Assess the morphology of the erythrocytes.
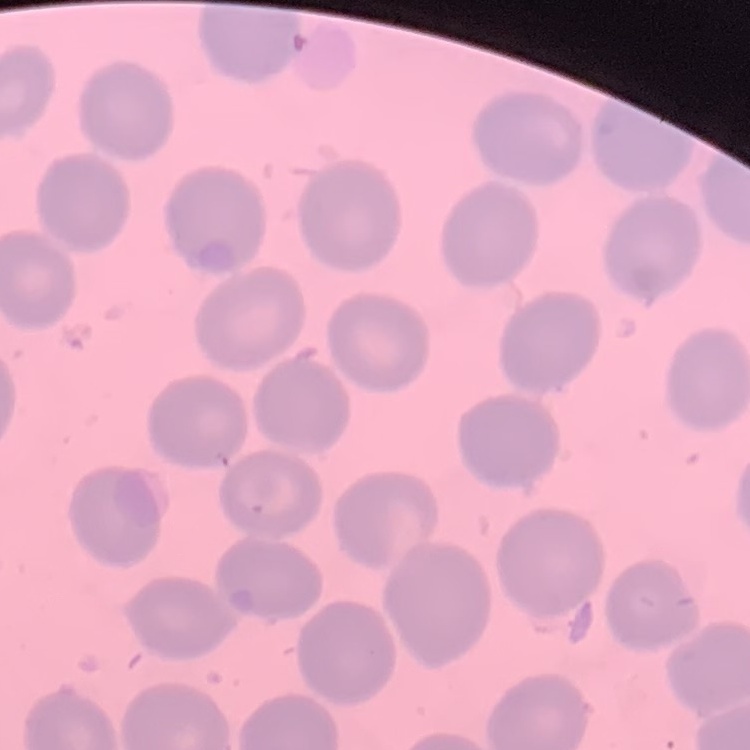
No rouleaux formation.

Square crop of a larger photomicrograph. Thin blood smear. Stained with either Field's or Giemsa.